Describe the morphology of the red blood cells.
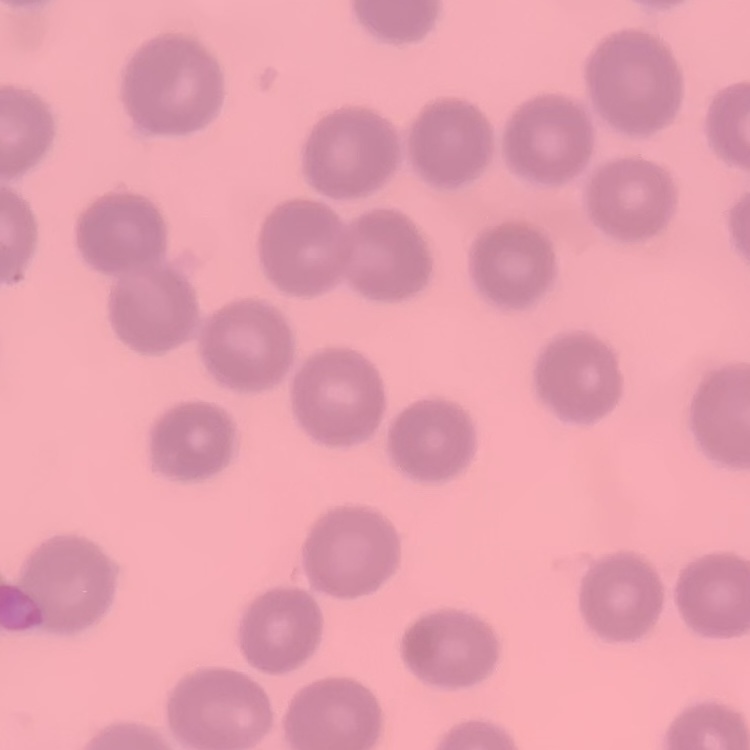
No rouleaux formation.

preparation = thin blood film
stain = Field's or Giemsa
image type = one tile cut from a larger photomicrograph